Describe the morphology of the red blood cells.
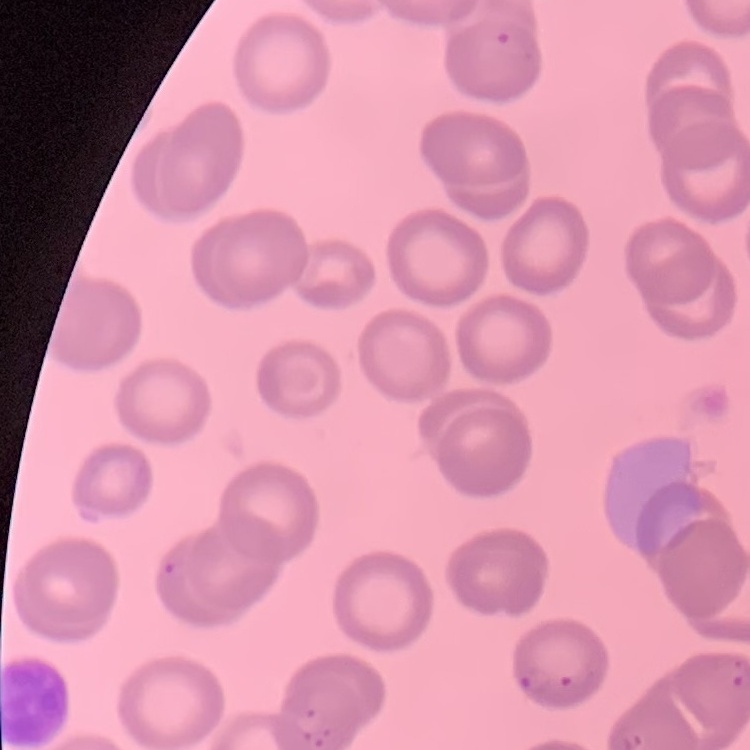
No rouleaux formation.

Field's or Giemsa stain. Square crop of a larger photomicrograph. Thin blood film.